Report the malaria status of this cell.
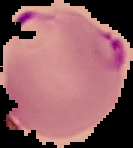
Parasitized.

Cell region segmented out of the field of view; the surrounding area is masked to black. Image is 133×148 pixels. From a thin blood smear.